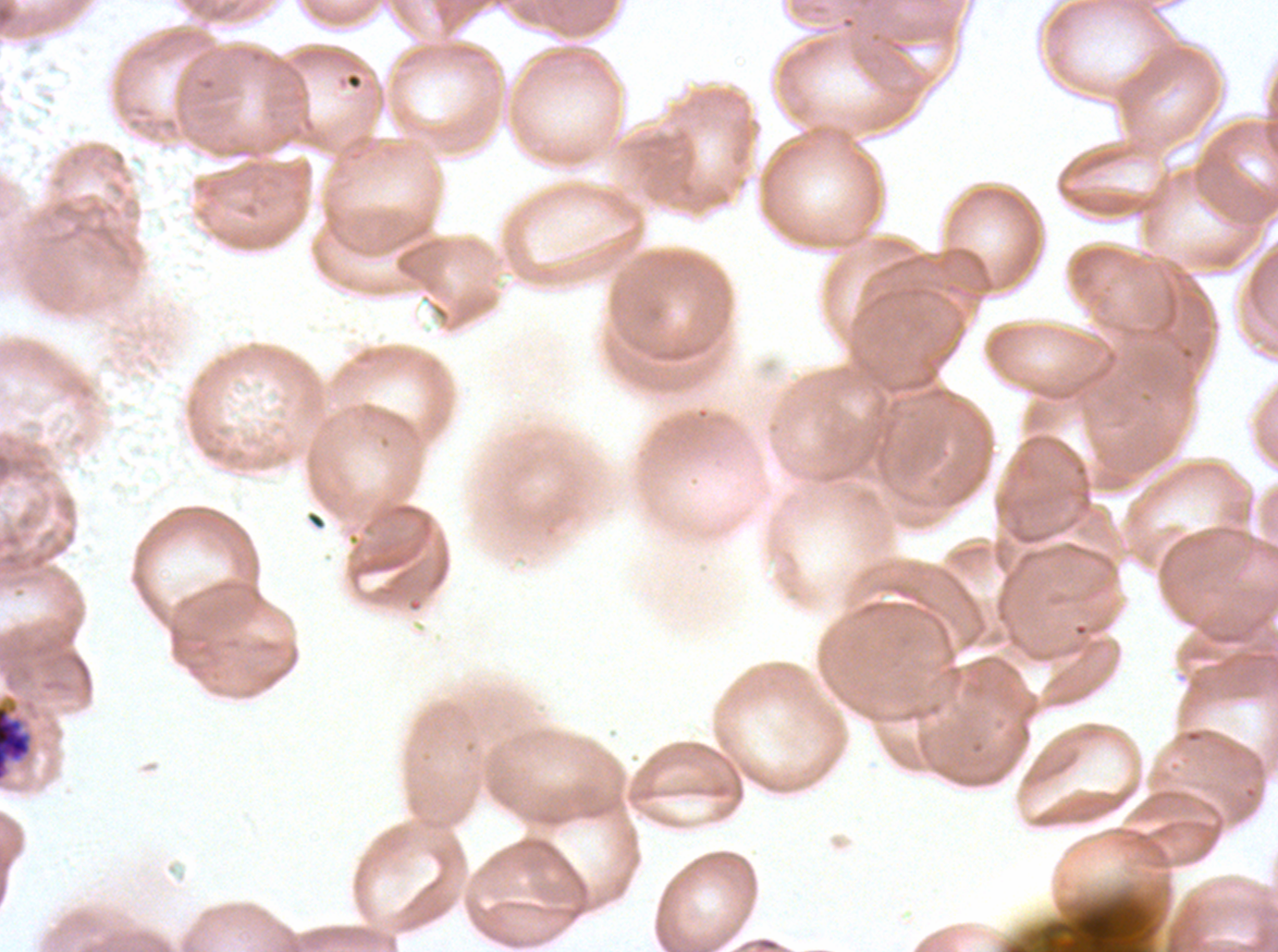
Approximate bounding boxes as (x1, y1, x2, y2) in pixels.
Summary:
  - Segmenter locations: (0, 697, 34, 783)
  - Specimen: Plasmodium falciparum from a patient in The Gambia, cultured ex vivo for 24 to 48 hours
  - Stain: Giemsa
  - Image size: 1278×952 pixels
  - Preparation: thin blood film
  - Field of view: sub-image separated from a larger composite